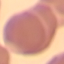

Summary:
  - Result: no malaria parasites detected
  - Stain: Giemsa
  - Image type: cell patch, automatically extracted from a larger field of view and resized to 64 × 64 pixels
  - Preparation: thin blood film
  - Capture: smartphone through the microscope eyepiece